Classify this cell by malaria status.
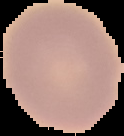
It is uninfected.

Summary:
  - Preparation: thin blood film
  - Image type: segmented cell region on a black background
  - Image size: 124×136 pixels